Locate and identify every blood parasite.
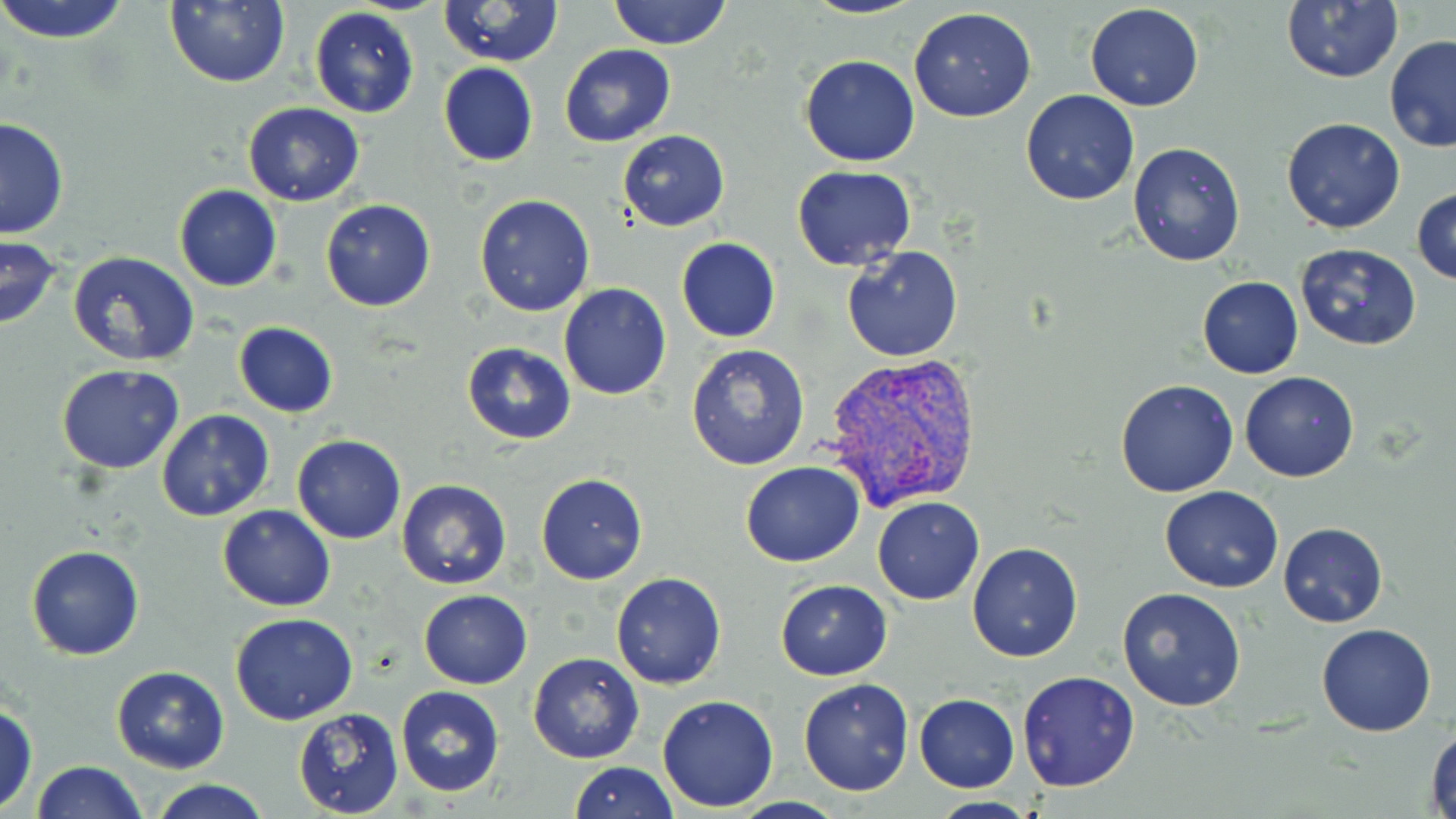
Approximate bounding boxes as [x1, y1, x2, y2] in pixels.
Plasmodium vivax-infected red blood cells: [818, 352, 986, 513].
No Plasmodium falciparum, Plasmodium ovale, Plasmodium malariae, Babesia divergens, or Trypanosoma brucei observed.

slide-level diagnosis = Plasmodium vivax
uninfected red blood cell locations = approximate bounding boxes as [x1, y1, x2, y2] in pixels: [0, 0, 132, 46], [167, 0, 290, 88], [439, 0, 562, 68], [608, 0, 731, 49], [802, 0, 927, 20], [1281, 1, 1403, 85], [1084, 4, 1206, 112], [310, 7, 418, 118], [909, 8, 1037, 123], [1385, 36, 1456, 154], [558, 44, 676, 147], [799, 54, 921, 167], [437, 63, 538, 166], [1020, 88, 1140, 205], [242, 102, 364, 206], [0, 117, 68, 241], [1280, 117, 1406, 234], [617, 129, 730, 231], [1128, 140, 1248, 268], [793, 166, 918, 272], [174, 184, 282, 292], [1412, 187, 1456, 287], [474, 193, 596, 317], [321, 199, 435, 312], [1, 235, 63, 332], [676, 237, 781, 343], [1295, 242, 1422, 351], [841, 246, 964, 364], [67, 252, 201, 368], [1210, 274, 1323, 458], [1197, 276, 1303, 378], [559, 284, 672, 400], [234, 322, 337, 417], [463, 344, 575, 443], [686, 344, 810, 469], [56, 363, 184, 473], [1240, 370, 1360, 483], [1115, 378, 1239, 497], [154, 411, 274, 522], [292, 434, 407, 543], [739, 462, 865, 567], [536, 472, 648, 585], [396, 478, 511, 590], [1160, 485, 1283, 593], [872, 496, 985, 605], [217, 505, 336, 611], [1278, 521, 1387, 627], [967, 540, 1083, 662], [26, 544, 145, 660], [610, 572, 727, 689], [774, 580, 892, 680], [1117, 588, 1246, 713], [419, 591, 531, 688], [230, 611, 359, 725], [1317, 622, 1437, 736], [528, 652, 644, 764], [112, 665, 229, 772], [1016, 670, 1141, 792], [798, 677, 915, 796], [395, 687, 504, 797], [657, 693, 780, 811], [914, 694, 1020, 792], [0, 702, 37, 814], [292, 708, 404, 817], [1427, 724, 1456, 817], [30, 760, 146, 819], [569, 762, 676, 818], [149, 777, 271, 818], [924, 796, 1040, 817]
modality = optical microscopy
field of view = one of a larger specimen
magnification = 1000x
preparation = thin blood smear
image size = 1456×819 pixels
stain = May-Grünwald-Giemsa